Evaluate for malaria.
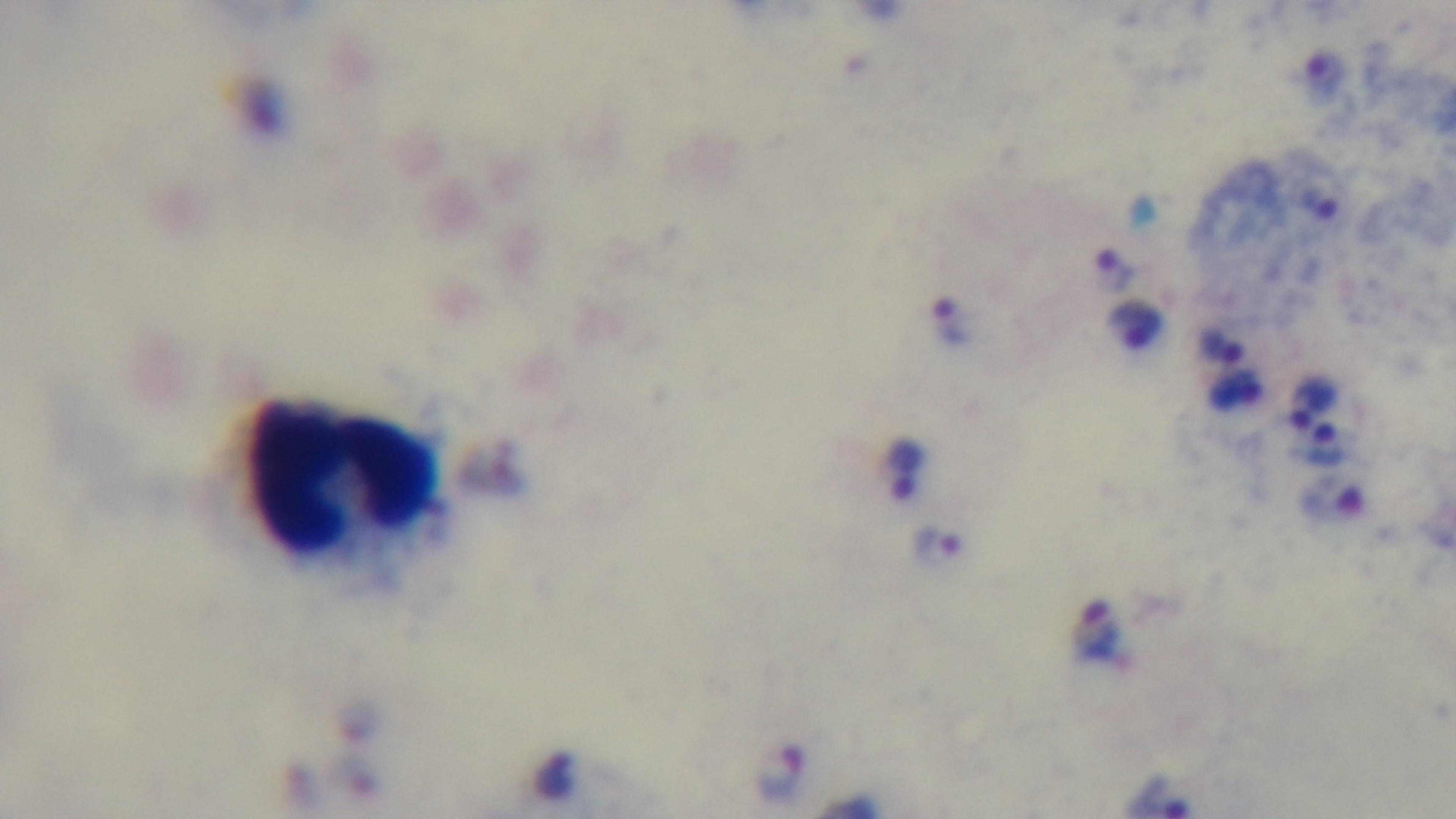

It is infected.

capture = mounted 4K digital camera
objective = 100x oil immersion
field of view = single
modality = light microscopy
stain = Giemsa
preparation = thick smear